Classify this cell by malaria status.
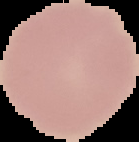
Uninfected.

Summary:
  - Preparation: thin blood film
  - Image type: segmented cell region on a black background
  - Image size: 139×142 pixels